Locate every leukocyte (white blood cell).
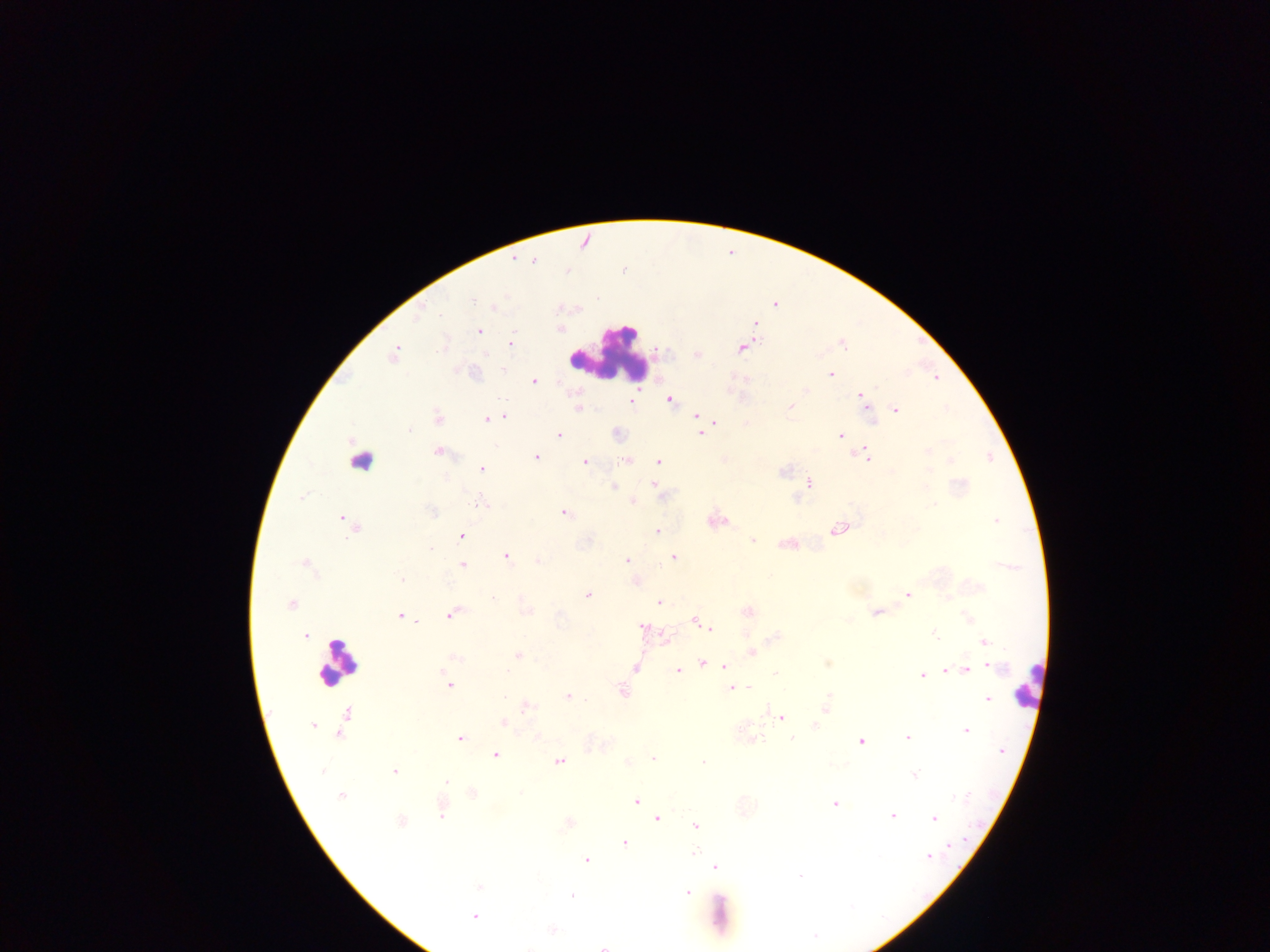
Approximate centers as (x, y) in pixels.
Leukocytes: (606, 354), (362, 453), (337, 664), (1029, 683).

Summary:
  - Plasmodium parasite locations: (513, 259), (534, 261), (597, 298), (472, 301), (494, 307), (756, 324), (559, 328), (478, 331), (510, 343), (843, 343), (741, 348), (393, 355), (696, 355), (831, 374), (534, 381), (806, 390), (862, 395), (670, 399), (631, 402), (791, 406), (577, 409), (895, 410), (696, 416), (504, 417), (437, 418), (486, 419), (715, 421), (409, 431), (701, 434), (558, 435), (840, 436), (927, 451), (438, 452), (866, 456), (536, 457), (626, 461), (658, 461), (951, 461), (585, 462), (482, 468), (929, 472), (808, 483), (652, 484), (613, 487), (302, 496), (633, 500), (479, 502), (933, 504), (431, 511), (565, 513), (343, 518), (996, 521), (347, 522), (352, 527), (838, 529), (657, 531), (462, 536), (752, 541), (430, 548), (507, 556), (673, 557), (626, 560), (538, 561), (304, 564), (462, 565), (402, 579), (636, 582), (588, 595), (908, 595), (493, 598), (659, 602), (292, 604), (526, 610), (747, 611), (876, 612), (451, 614), (400, 616), (415, 621), (695, 621), (643, 627), (710, 628), (934, 634), (305, 635), (775, 637), (986, 642), (752, 652), (519, 656), (456, 658), (703, 664), (828, 664), (724, 666), (993, 667), (636, 668), (967, 669), (677, 671), (945, 671), (775, 673), (922, 675), (449, 685), (731, 688), (749, 688), (622, 691), (568, 696), (828, 696), (504, 697), (987, 699), (527, 707), (825, 709), (766, 710), (781, 717), (504, 723), (312, 725), (815, 725), (966, 731), (907, 737), (792, 738), (460, 739), (752, 739), (861, 741), (1003, 751), (495, 755), (653, 759), (559, 762), (628, 762), (703, 763), (323, 770), (395, 770), (915, 774), (447, 783), (473, 792), (340, 795), (636, 802), (834, 804), (442, 814), (891, 816), (934, 818), (657, 819), (401, 822), (695, 826), (625, 843), (950, 845), (693, 854), (929, 856), (586, 860), (715, 867), (800, 875), (479, 887), (688, 893), (572, 896), (474, 917), (552, 929), (603, 947)
  - Image size: 1270×952 pixels
  - Preparation: thick blood film
  - Country: Ghana
  - Field of view: single
  - Capture: mobile-phone photograph through a microscope